Identify the parasite.
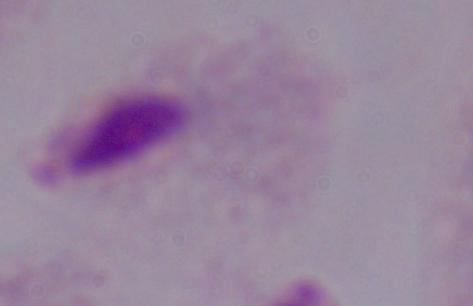

A trichomonad.

magnification = 1000x
modality = micrograph